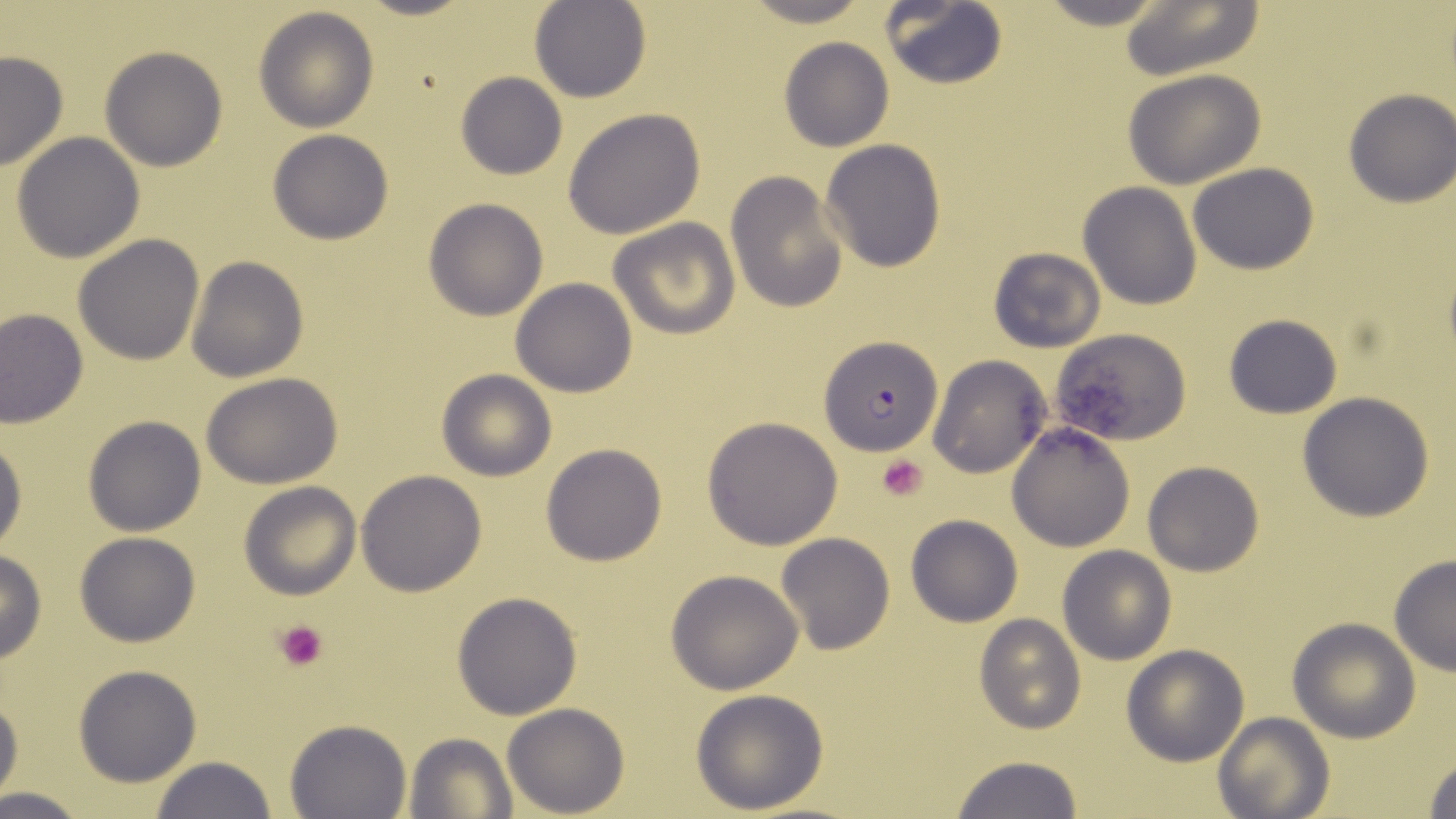
slide-level diagnosis = Plasmodium falciparum
uninfected red blood cell locations = approximate bounding boxes as (x1, y1, x2, y2) in pixels: (530, 0, 651, 103), (736, 0, 878, 27), (1032, 0, 1174, 30), (1118, 0, 1264, 83), (878, 1, 1007, 89), (252, 6, 378, 132), (778, 36, 894, 153), (100, 46, 228, 171), (0, 50, 69, 172), (1123, 69, 1267, 189), (456, 71, 567, 180), (1342, 90, 1455, 207), (562, 107, 706, 239), (266, 129, 394, 244), (11, 131, 147, 263), (819, 140, 946, 271), (1188, 162, 1318, 275), (726, 172, 848, 312), (1077, 182, 1202, 309), (423, 197, 548, 321), (609, 218, 739, 339), (72, 233, 205, 366), (986, 246, 1106, 354), (187, 255, 309, 383), (510, 277, 638, 396), (1, 308, 87, 427), (1224, 314, 1342, 419), (1052, 328, 1192, 447), (927, 355, 1050, 479), (435, 369, 557, 480), (202, 372, 344, 488), (1298, 391, 1436, 521), (700, 415, 845, 550), (83, 416, 207, 536), (1007, 423, 1136, 552), (0, 432, 26, 557), (541, 444, 668, 566), (1142, 460, 1264, 577), (356, 470, 487, 596), (240, 482, 361, 600), (906, 514, 1023, 627), (74, 531, 200, 647), (775, 532, 896, 656), (1057, 545, 1177, 664), (0, 550, 47, 664), (1388, 554, 1456, 675), (664, 569, 806, 695), (450, 591, 583, 720), (975, 615, 1084, 733), (1287, 617, 1420, 741), (1121, 644, 1249, 767), (73, 664, 200, 787), (690, 688, 830, 814), (0, 693, 23, 799), (502, 702, 628, 816), (1212, 712, 1333, 819), (286, 718, 412, 819), (404, 731, 515, 817), (1421, 751, 1456, 818), (950, 755, 1084, 819), (149, 756, 278, 819), (0, 786, 92, 818)
magnification = 1000x
image size = 1456×819 pixels
preparation = thin blood film
stain = May-Grünwald-Giemsa
platelet locations = approximate bounding boxes as (x1, y1, x2, y2) in pixels: (876, 454, 929, 501), (275, 618, 330, 671)
modality = optical microscopy
Plasmodium falciparum-infected red blood cell locations = approximate bounding boxes as (x1, y1, x2, y2) in pixels: (820, 336, 942, 454)
field of view = single